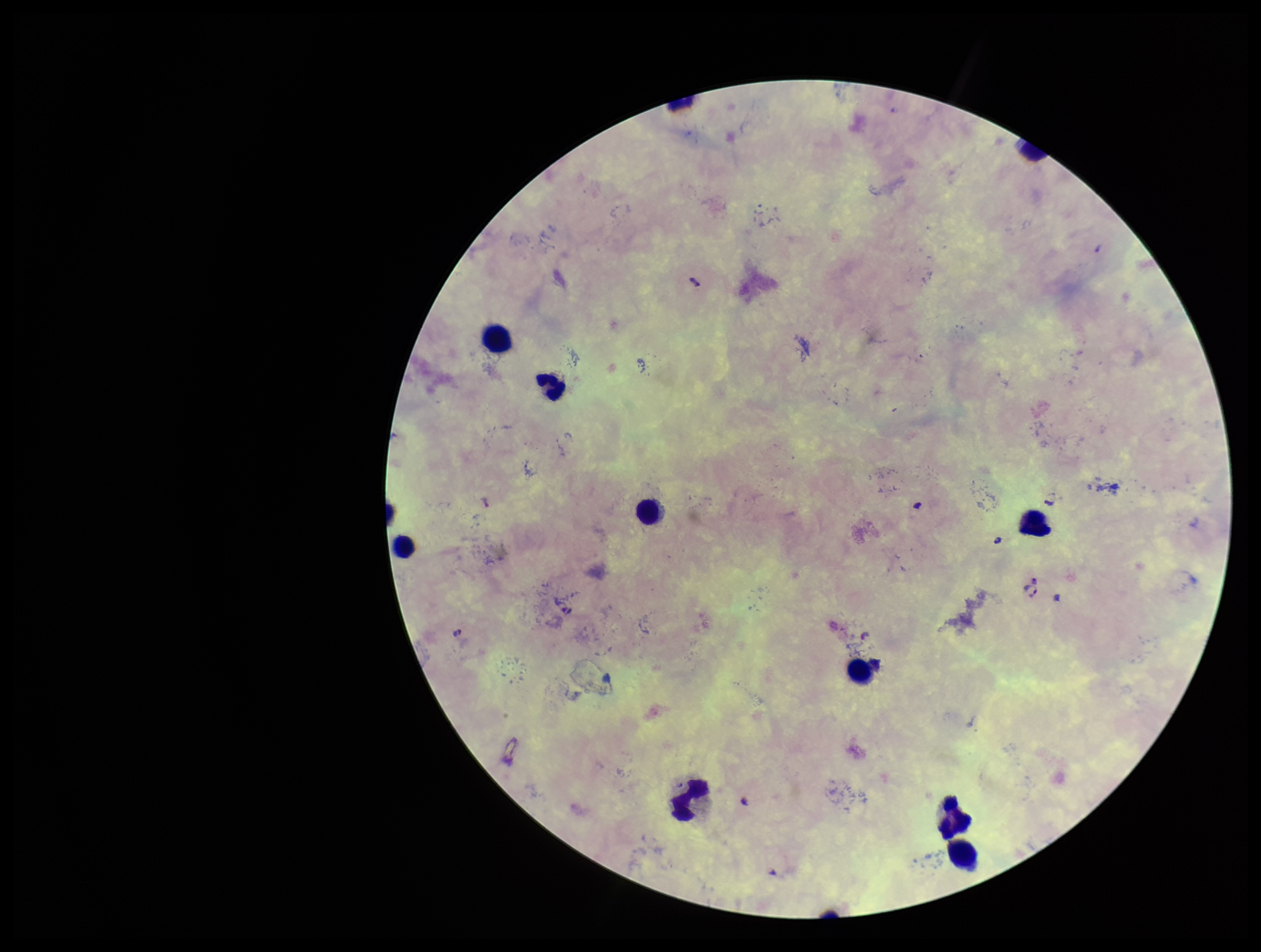

Leukocyte count: 10. Species reported for this patient: Plasmodium falciparum. Smartphone photograph taken through the eyepiece of a microscope. Parasite count: 4. One field from this slide. Giemsa stain. Plasmodium parasites: detected. Preparation: thick blood smear. Patient malaria status: infected. Image is 1261×952 pixels.